Give the extent of all white blood cells.
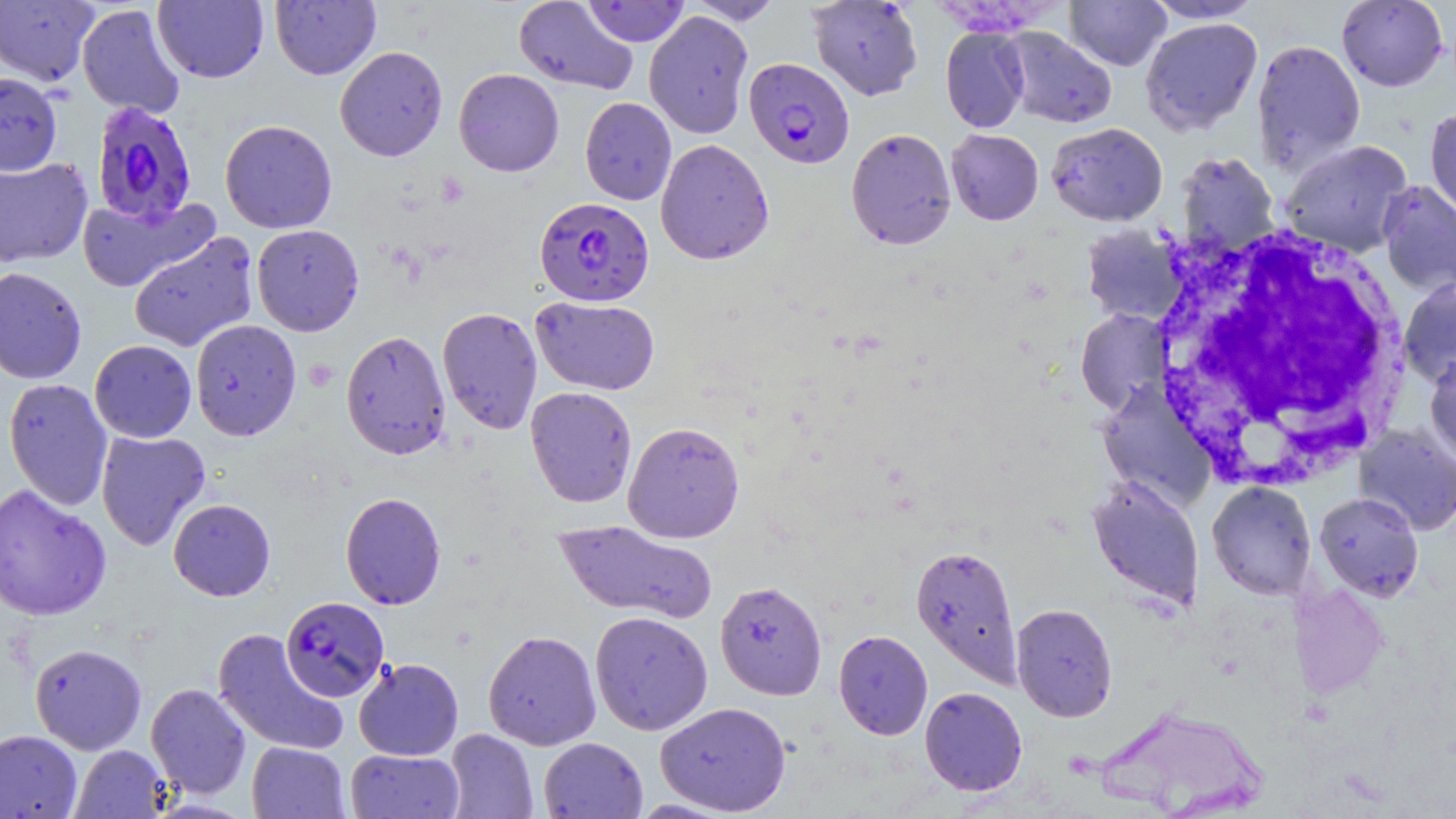
Approximate bounding boxes as (x1,y1)-(x2,y2) corner pairs in pixels.
White blood cells: (1148,220)-(1412,489).

Summary:
  - Uninfected red blood cell locations: (686,0)-(784,24), (808,0)-(923,101), (1065,0)-(1171,71), (1144,0)-(1264,23), (0,1)-(99,86), (153,1)-(269,83), (270,1)-(381,80), (513,1)-(639,95), (582,1)-(690,47), (1336,1)-(1449,91), (77,3)-(186,119), (643,10)-(754,139), (1140,17)-(1263,135), (940,26)-(1030,133), (1001,27)-(1117,128), (1251,38)-(1366,175), (335,46)-(448,161), (454,68)-(564,177), (0,71)-(63,176), (580,97)-(676,205), (1424,106)-(1456,225), (220,118)-(337,234), (1046,122)-(1167,227), (845,127)-(956,250), (945,129)-(1044,225), (655,138)-(774,265), (1280,139)-(1412,258), (1176,151)-(1280,258), (0,156)-(93,268), (1377,181)-(1456,297), (76,194)-(219,293), (1080,223)-(1188,326), (251,224)-(364,336), (129,232)-(259,352), (0,266)-(87,384), (1398,276)-(1456,387), (530,296)-(660,395), (437,307)-(543,435), (1075,309)-(1171,415), (190,319)-(301,440), (341,330)-(451,460), (89,339)-(197,443), (1424,352)-(1456,467), (3,377)-(113,511), (1096,383)-(1216,511), (525,386)-(638,508), (622,421)-(745,543), (1354,424)-(1456,536), (95,429)-(211,550), (1086,475)-(1205,610), (1206,481)-(1316,601), (0,484)-(112,622), (340,492)-(446,610), (1315,492)-(1424,601), (168,498)-(276,601), (554,519)-(718,624), (911,543)-(1022,687), (714,580)-(827,700), (1290,581)-(1388,699), (1011,603)-(1118,722), (589,611)-(713,735), (212,628)-(349,756), (483,630)-(601,750), (834,630)-(933,739), (30,643)-(147,754), (353,657)-(464,761), (146,682)-(251,798), (920,687)-(1027,796), (654,701)-(791,816), (1095,703)-(1267,817), (0,729)-(82,819), (444,729)-(538,818), (538,737)-(648,819), (247,741)-(350,819), (70,744)-(171,818), (345,749)-(465,818)
  - Plasmodium falciparum-infected red blood cell locations: (744,57)-(854,168), (90,101)-(198,225), (535,196)-(654,306), (280,596)-(389,702)
  - Slide-level diagnosis: Plasmodium falciparum
  - Preparation: thin blood film
  - Image size: 1456×819 pixels
  - Modality: optical microscopy
  - Stain: May-Grünwald-Giemsa
  - Magnification: 1000x
  - Field of view: one of a larger specimen